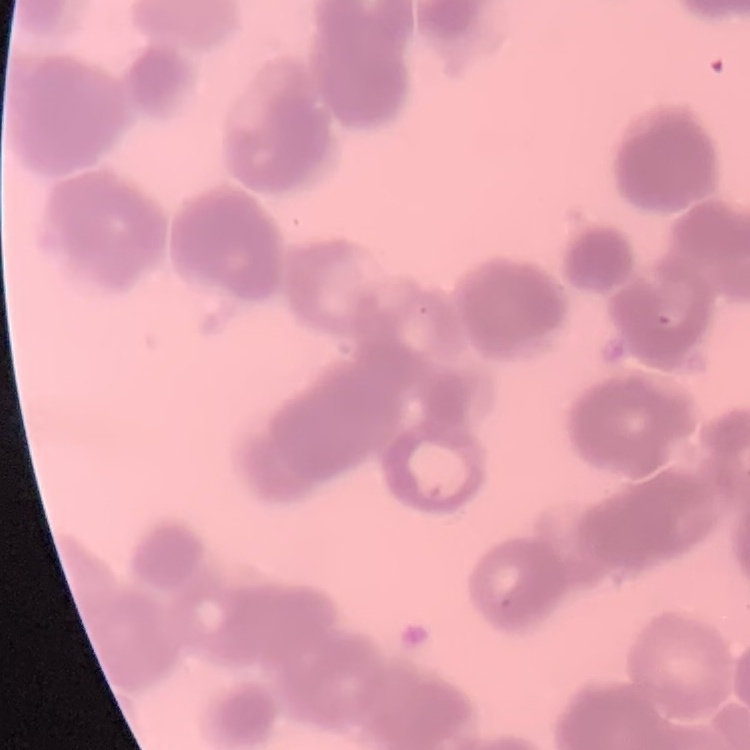
The erythrocytes show rouleaux formation. Field's or Giemsa stain. Square crop of a larger photomicrograph. Thin blood film.